Give the extent of all Plasmodium ovale-infected red blood cells.
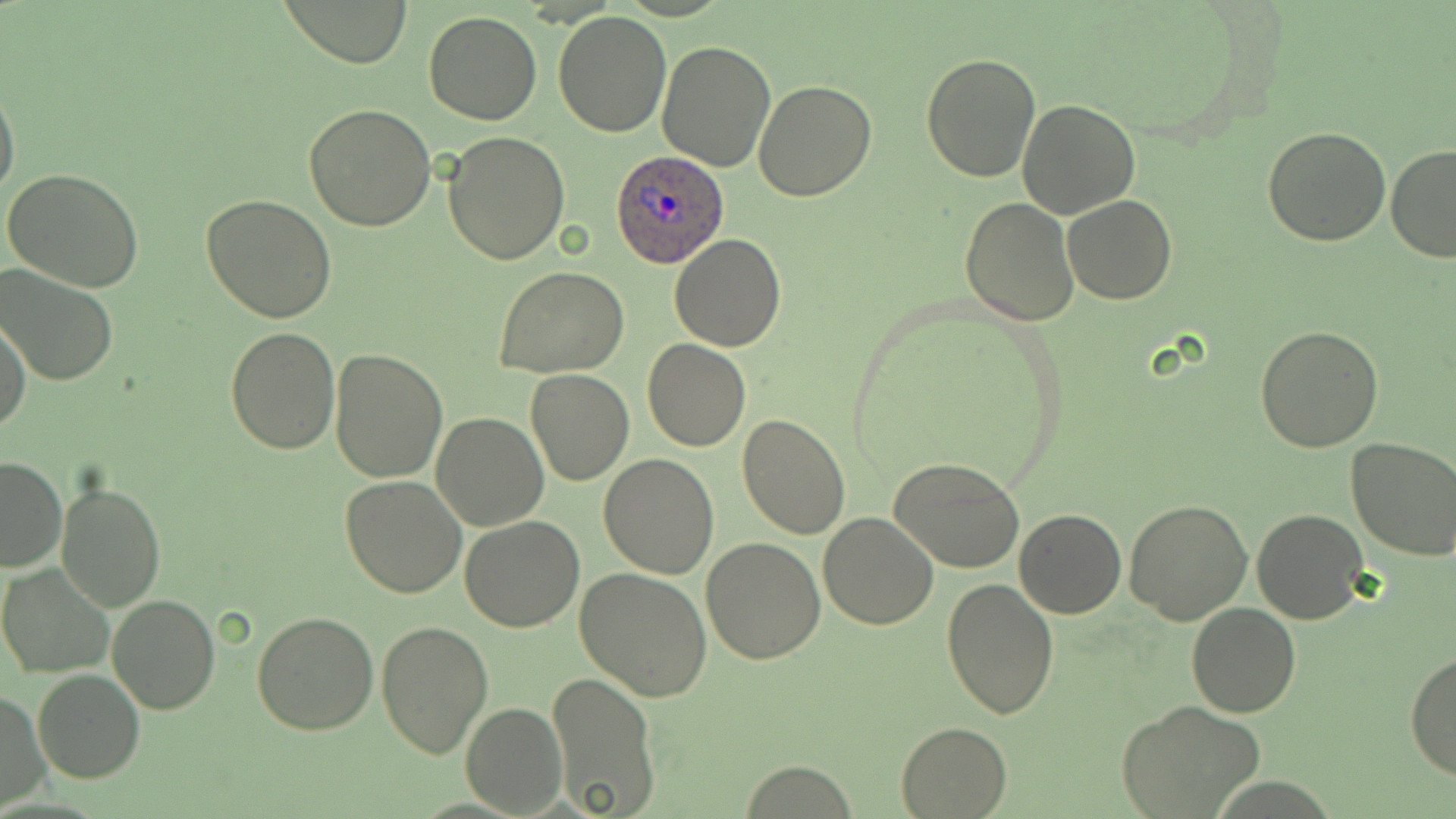
Approximate bounding boxes as [x1, y1, x2, y2] in pixels.
Plasmodium ovale-infected red blood cells: [608, 149, 730, 268].

Uninfected red blood cell locations: [279, 0, 412, 67], [552, 10, 672, 137], [424, 12, 542, 124], [656, 41, 776, 171], [920, 53, 1042, 182], [0, 81, 20, 203], [753, 81, 878, 201], [1017, 98, 1142, 220], [304, 104, 438, 230], [1262, 126, 1391, 246], [441, 131, 569, 265], [1386, 145, 1456, 264], [4, 167, 145, 293], [202, 194, 337, 322], [1063, 196, 1178, 304], [959, 197, 1079, 326], [669, 233, 786, 352], [0, 265, 120, 387], [496, 267, 627, 379], [0, 314, 30, 435], [1256, 323, 1384, 451], [226, 325, 340, 453], [643, 341, 750, 451], [329, 350, 447, 483], [525, 368, 634, 486], [432, 411, 548, 530], [737, 413, 851, 541], [1344, 436, 1456, 561], [598, 453, 719, 579], [890, 454, 1026, 572], [0, 455, 66, 571], [340, 475, 467, 598], [57, 481, 166, 611], [1124, 498, 1253, 626], [1014, 507, 1126, 618], [1251, 509, 1367, 625], [819, 511, 938, 629], [459, 516, 584, 631], [699, 537, 826, 664], [1, 563, 116, 679], [574, 567, 712, 701], [941, 578, 1060, 720], [107, 595, 221, 714], [1186, 602, 1301, 717], [252, 610, 380, 736], [374, 618, 493, 760], [1406, 651, 1456, 780], [33, 669, 145, 782], [546, 670, 660, 816], [1, 689, 49, 810], [1119, 700, 1266, 819], [461, 703, 565, 816], [895, 720, 1013, 818], [739, 762, 859, 817]. Slide-level diagnosis: Plasmodium ovale. May-Grünwald-Giemsa-stained preparation. Light microscopy. One field of a larger specimen. Image is 1456×819 pixels. Captured at 1000x magnification. Thin blood film.